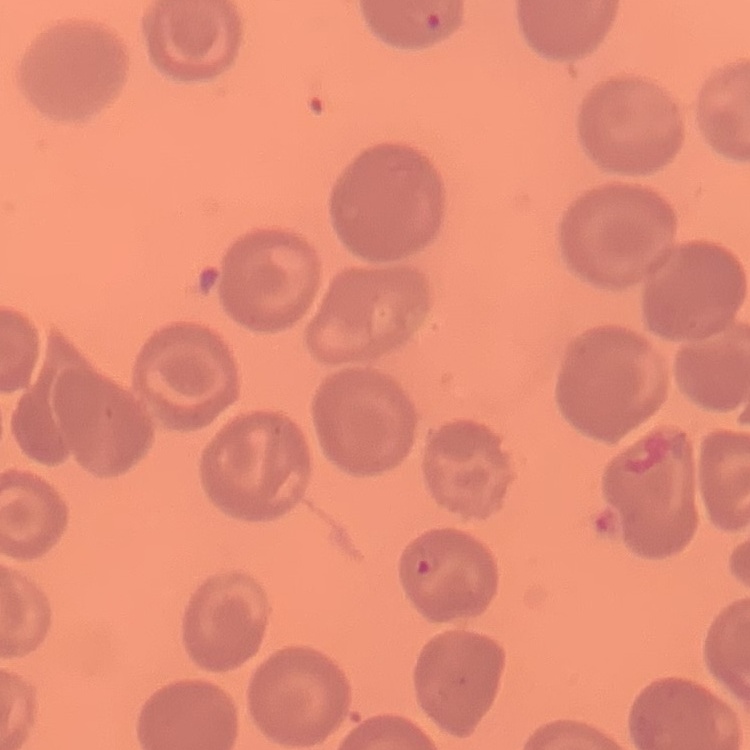

Summary:
  - Erythrocyte morphology: no rouleaux formation
  - Image type: one tile cut from a larger photomicrograph
  - Stain: Field's or Giemsa
  - Preparation: thin blood smear